Classify this cell by malaria status.
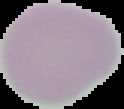

It is uninfected.

Summary:
  - Image type: segmented cell region on a black background
  - Image size: 124×109 pixels
  - Preparation: thin blood film